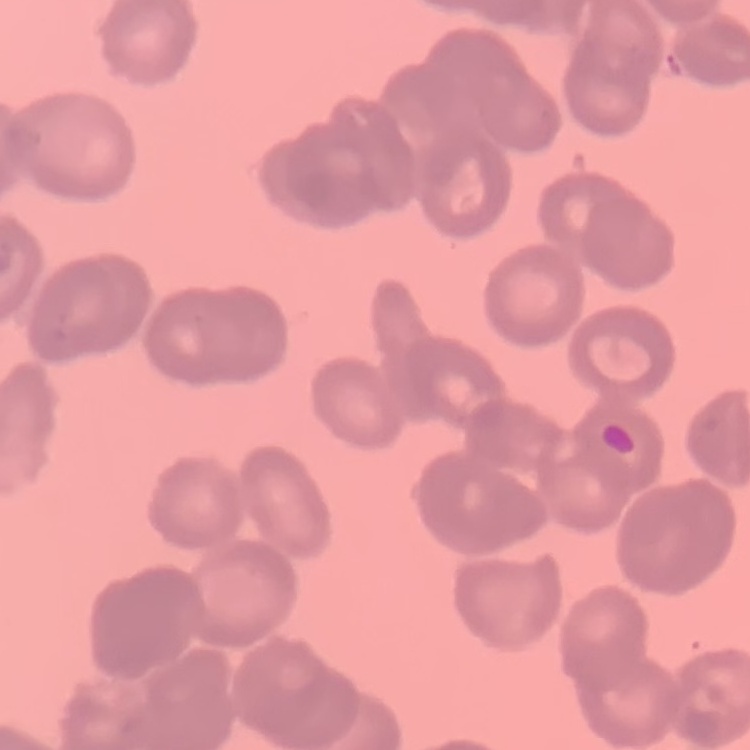 The erythrocytes show rouleaux formation. Field's or Giemsa stain. Square crop of a larger photomicrograph. Thin peripheral smear.